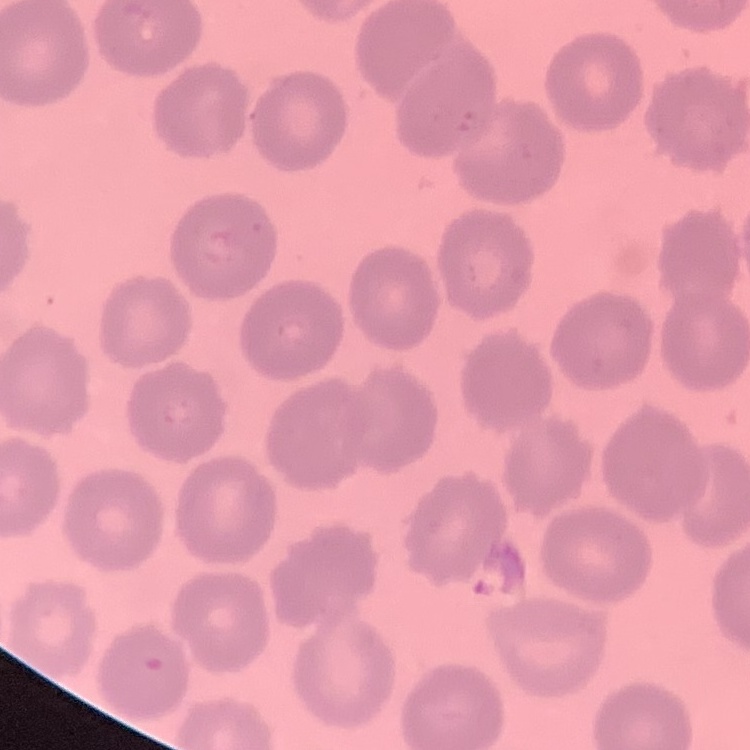
red blood cell morphology = no rouleaux formation
preparation = thin blood smear
stain = Field's or Giemsa
image type = square crop of a larger photomicrograph